Report the malaria status of this cell.
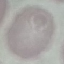

It is uninfected.

Giemsa stain. Acquired by smartphone through the microscope eyepiece. Thin smear of blood. Cell patch, automatically extracted from a larger field of view and resized to 64 × 64 pixels.